Report the malaria status of this cell.
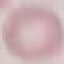
It is uninfected.

{
  "stain": "Giemsa",
  "image_type": "cell patch, automatically extracted from a larger field of view and resized to 64 × 64 pixels",
  "preparation": "thin smear",
  "capture": "smartphone camera at the microscope eyepiece"
}